Report the malaria status of this cell.
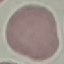
Uninfected.

Summary:
  - Image type: cell patch, automatically extracted from a larger field of view and resized to 64 × 64 pixels
  - Capture: smartphone camera at the microscope eyepiece
  - Preparation: thin blood smear
  - Stain: Giemsa